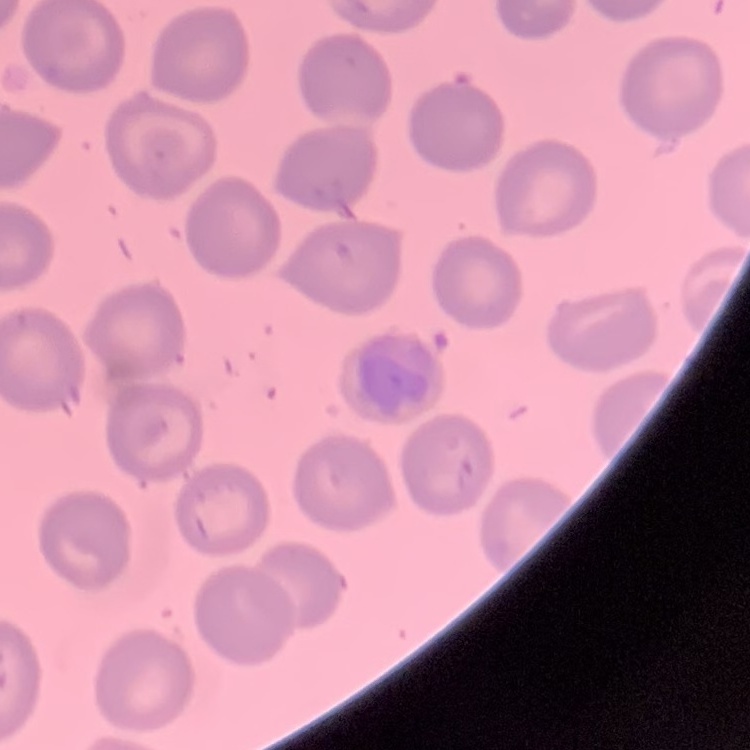

Summary:
  - Erythrocyte morphology: no rouleaux formation
  - Image type: square crop of a larger photomicrograph
  - Stain: Field's or Giemsa
  - Preparation: thin peripheral smear